Assess this cell for malaria.
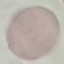
It is uninfected.

stain = Giemsa
preparation = thin blood smear
image type = automatically extracted cell patch, resized to 64 × 64 pixels
capture = smartphone through the microscope eyepiece